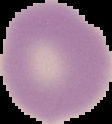 From a thin blood smear. Cell region segmented out of the field of view; the surrounding area is masked to black. Image is 112×124 pixels. Malaria status: uninfected.